Give the preparation type.
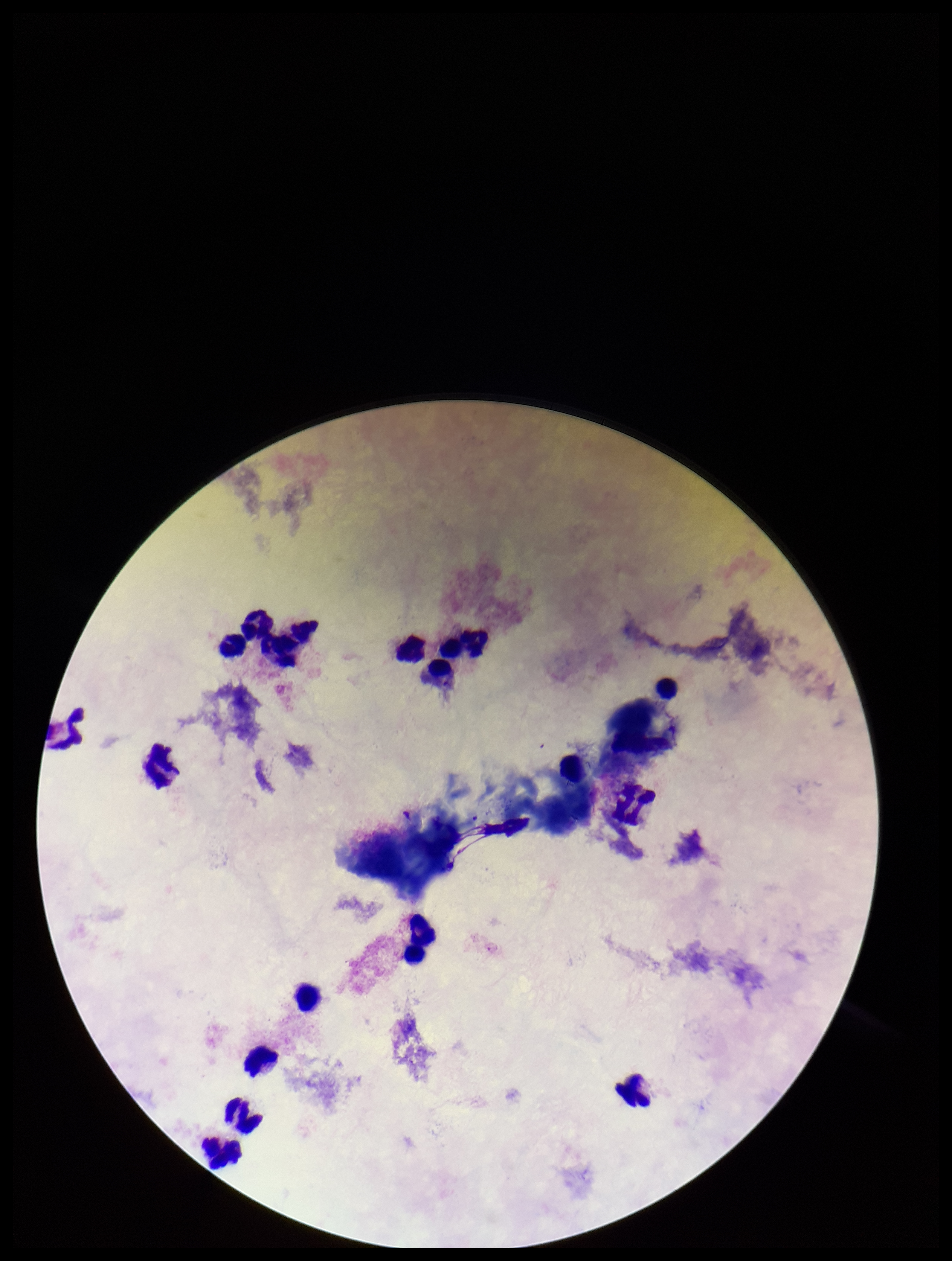
It is a thick blood smear.

One field from this slide. Leukocyte count: 15. Plasmodium parasites: none seen. Smartphone photograph taken through the eyepiece of a microscope. Parasite count: 0. Image is 952×1261 pixels. Patient malaria status: negative. Giemsa stain.